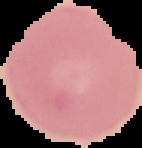
result = no malaria parasites detected
image size = 142×148 pixels
image type = segmented cell region with the area outside set to black
preparation = thin blood film